Assess this cell for malaria.
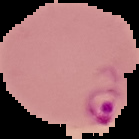

It is parasitized.

From a thin blood smear. The area outside the segmented cell region is set to black. Image is 139×139 pixels.